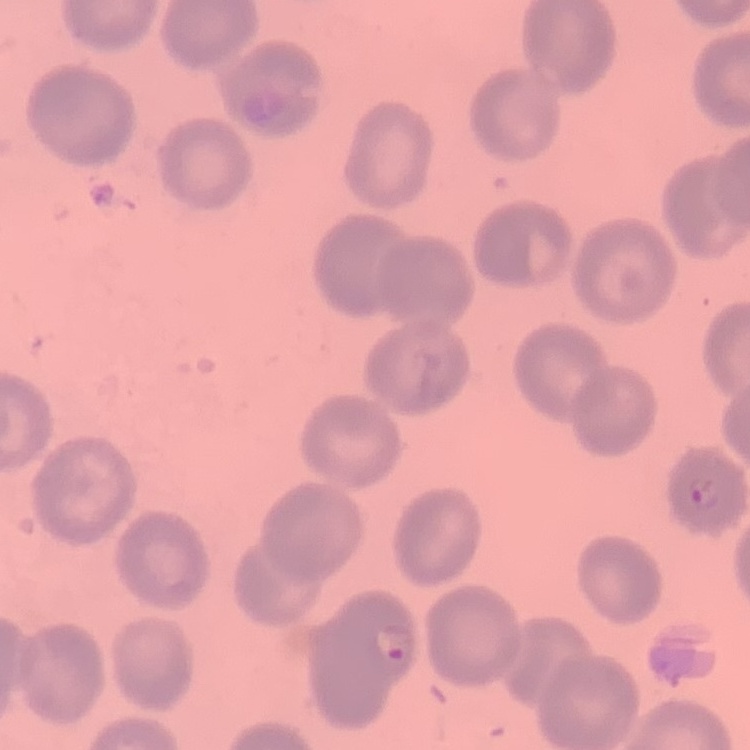

erythrocyte morphology = no rouleaux formation
preparation = thin peripheral smear
image type = square crop of a larger photomicrograph
stain = Field's or Giemsa